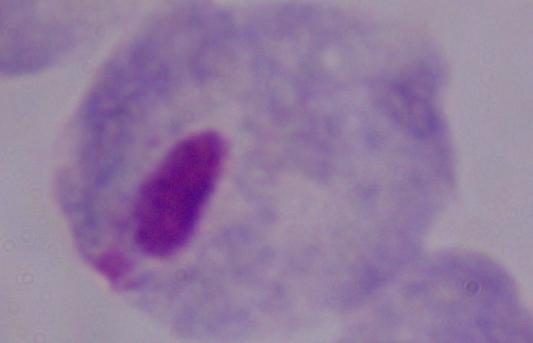
{
  "magnification": "1000x",
  "modality": "photomicrograph",
  "identification": "trichomonad"
}